Classify this cell by malaria status.
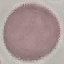
It is uninfected.

Summary:
  - Stain: Giemsa
  - Capture: smartphone through the microscope eyepiece
  - Preparation: thin smear
  - Image type: automatically extracted cell patch, resized to 64 × 64 pixels